Locate every uninfected red blood cell.
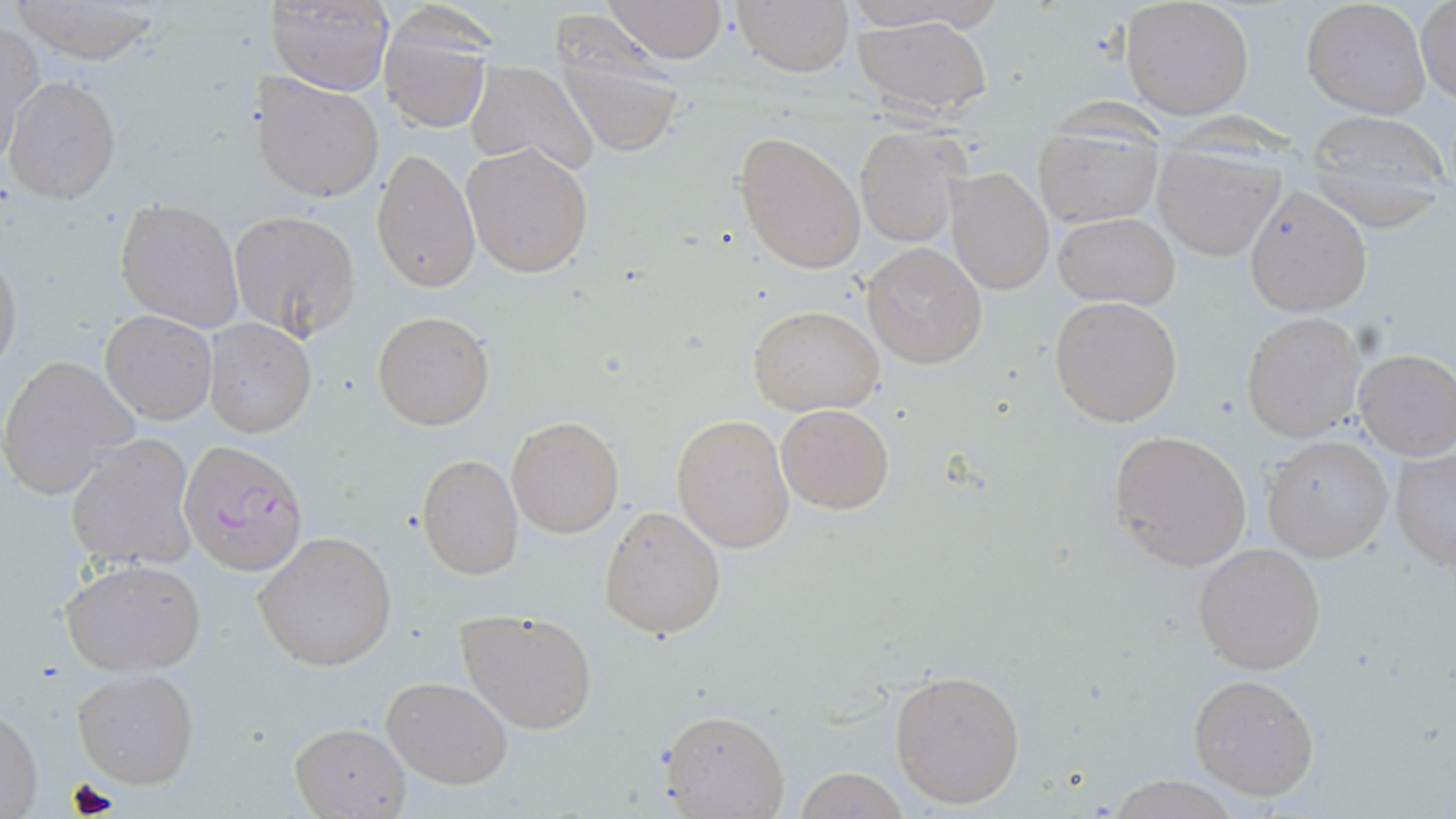
Approximate bounding boxes as named x1/y1/x2/y2 corners in pixels.
Uninfected red blood cells: (x1=8, y1=0, x2=171, y2=63), (x1=602, y1=0, x2=729, y2=65), (x1=732, y1=0, x2=852, y2=77), (x1=840, y1=0, x2=993, y2=31), (x1=1302, y1=0, x2=1432, y2=119), (x1=1415, y1=1, x2=1455, y2=106), (x1=267, y1=2, x2=394, y2=94), (x1=1121, y1=2, x2=1253, y2=120), (x1=853, y1=15, x2=993, y2=117), (x1=379, y1=18, x2=491, y2=131), (x1=1, y1=22, x2=44, y2=158), (x1=554, y1=28, x2=687, y2=158), (x1=466, y1=61, x2=599, y2=176), (x1=253, y1=74, x2=384, y2=204), (x1=4, y1=75, x2=121, y2=204), (x1=1306, y1=111, x2=1447, y2=223), (x1=1032, y1=122, x2=1162, y2=227), (x1=853, y1=125, x2=969, y2=247), (x1=734, y1=130, x2=866, y2=272), (x1=462, y1=143, x2=594, y2=278), (x1=372, y1=146, x2=479, y2=295), (x1=1153, y1=147, x2=1282, y2=259), (x1=946, y1=168, x2=1053, y2=295), (x1=1245, y1=185, x2=1372, y2=316), (x1=115, y1=200, x2=243, y2=329), (x1=229, y1=209, x2=360, y2=340), (x1=1054, y1=212, x2=1181, y2=308), (x1=862, y1=242, x2=988, y2=369), (x1=0, y1=250, x2=22, y2=379), (x1=1048, y1=295, x2=1185, y2=427), (x1=749, y1=305, x2=883, y2=416), (x1=372, y1=310, x2=494, y2=428), (x1=101, y1=311, x2=216, y2=424), (x1=1241, y1=313, x2=1363, y2=441), (x1=203, y1=318, x2=315, y2=438), (x1=1354, y1=351, x2=1456, y2=461), (x1=0, y1=354, x2=141, y2=500), (x1=775, y1=403, x2=895, y2=515), (x1=672, y1=414, x2=795, y2=552), (x1=507, y1=417, x2=625, y2=538), (x1=1107, y1=430, x2=1253, y2=572), (x1=66, y1=433, x2=197, y2=570), (x1=1263, y1=435, x2=1393, y2=563), (x1=1390, y1=446, x2=1456, y2=570), (x1=417, y1=454, x2=523, y2=578), (x1=598, y1=505, x2=726, y2=638), (x1=253, y1=530, x2=398, y2=671), (x1=1193, y1=542, x2=1327, y2=674), (x1=61, y1=560, x2=206, y2=676), (x1=456, y1=609, x2=598, y2=735), (x1=73, y1=667, x2=198, y2=788), (x1=887, y1=670, x2=1028, y2=809), (x1=1188, y1=673, x2=1320, y2=801), (x1=382, y1=675, x2=512, y2=788), (x1=0, y1=706, x2=43, y2=819), (x1=660, y1=708, x2=790, y2=817), (x1=289, y1=722, x2=411, y2=817), (x1=789, y1=766, x2=913, y2=819), (x1=1106, y1=776, x2=1242, y2=817).

Plasmodium falciparum-infected red blood cell locations: (x1=179, y1=440, x2=307, y2=575). Slide-level diagnosis: Plasmodium falciparum. Light microscopy. May-Grünwald-Giemsa stain. Image is 1456×819 pixels. Captured at 1000x magnification. One field of a larger specimen. Thin blood smear.